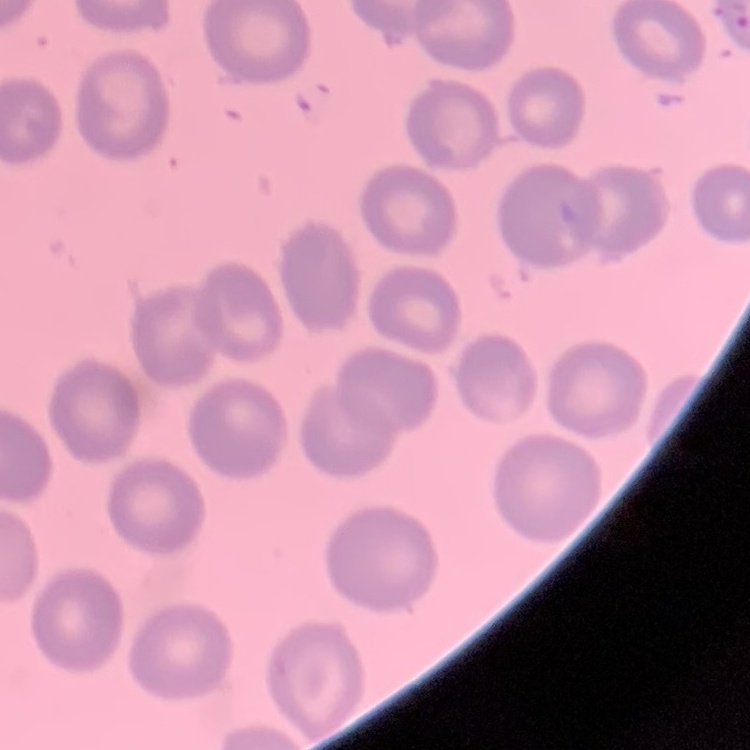

Summary:
  - Erythrocyte morphology: no rouleaux formation
  - Image type: one tile cut from a larger photomicrograph
  - Preparation: thin blood film
  - Stain: Field's or Giemsa